Give the extent of all Plasmodium ovale-infected red blood cells.
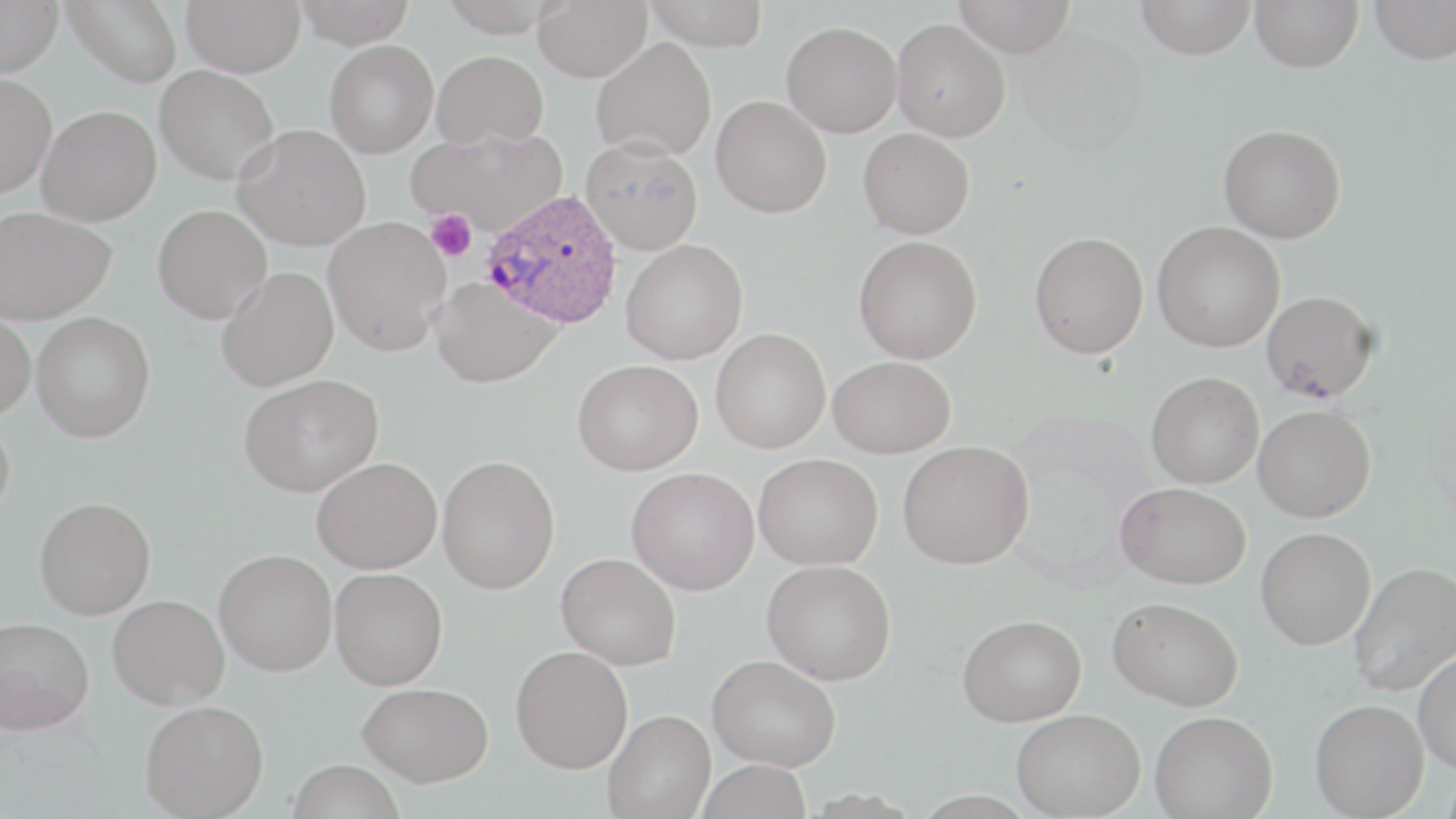
Approximate bounding boxes as (x1,y1)-(x2,y2) corner pairs in pixels.
Plasmodium ovale-infected red blood cells: (482,188)-(623,329).

{
  "slide_level_diagnosis": "Plasmodium ovale",
  "platelet_locations": "approximate bounding boxes as (x1,y1)-(x2,y2) corner pairs in pixels: (426,209)-(476,262)",
  "uninfected_red_blood_cell_locations": "approximate bounding boxes as (x1,y1)-(x2,y2) corner pairs in pixels: (0,0)-(63,77), (63,0)-(183,87), (182,0)-(306,77), (293,0)-(418,48), (533,0)-(652,82), (643,0)-(770,49), (954,0)-(1075,58), (1136,0)-(1256,60), (1250,0)-(1363,73), (1369,0)-(1456,64), (892,18)-(1011,141), (782,21)-(903,137), (1019,28)-(1148,156), (591,37)-(716,161), (324,39)-(439,158), (432,50)-(549,149), (154,65)-(280,185), (0,72)-(57,198), (711,96)-(832,218), (36,105)-(161,226), (233,124)-(372,250), (1218,125)-(1345,243), (858,127)-(975,239), (408,128)-(567,234), (581,138)-(703,254), (152,204)-(272,324), (0,207)-(116,324), (323,216)-(451,355), (1152,221)-(1285,353), (1029,230)-(1149,359), (853,235)-(982,364), (620,239)-(748,365), (217,266)-(339,391), (429,277)-(560,388), (1261,290)-(1380,402), (0,309)-(36,420), (31,312)-(155,442), (711,328)-(831,453), (828,356)-(955,459), (572,359)-(703,475), (1146,371)-(1264,488), (238,373)-(383,496), (1253,404)-(1376,522), (0,415)-(15,522), (898,440)-(1034,569), (753,453)-(883,570), (437,455)-(560,593), (311,457)-(442,573), (627,467)-(759,595), (1115,481)-(1251,589), (35,497)-(156,618), (1256,526)-(1375,649), (214,549)-(337,676), (556,552)-(681,670), (762,559)-(896,684), (1349,561)-(1456,696), (330,567)-(448,690), (107,595)-(229,709), (1107,596)-(1243,710), (957,614)-(1087,726), (0,615)-(94,735), (510,645)-(633,773), (1414,649)-(1456,773), (708,654)-(841,771), (357,681)-(493,787), (1310,699)-(1429,818), (140,700)-(269,818), (1011,708)-(1145,818), (603,709)-(716,819), (1150,710)-(1277,818), (696,758)-(813,819), (286,759)-(405,819)",
  "field_of_view": "one of a larger specimen",
  "image_size": "1456×819 pixels",
  "modality": "light microscopy",
  "stain": "May-Grünwald-Giemsa",
  "preparation": "thin blood film",
  "magnification": "1000x"
}